State which cell type is depicted.
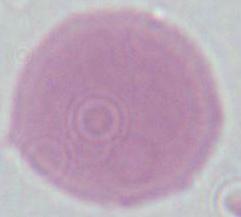
An erythrocyte.

magnification: 1000x
modality: micrograph